Point out each Plasmodium parasite and each leukocyte.
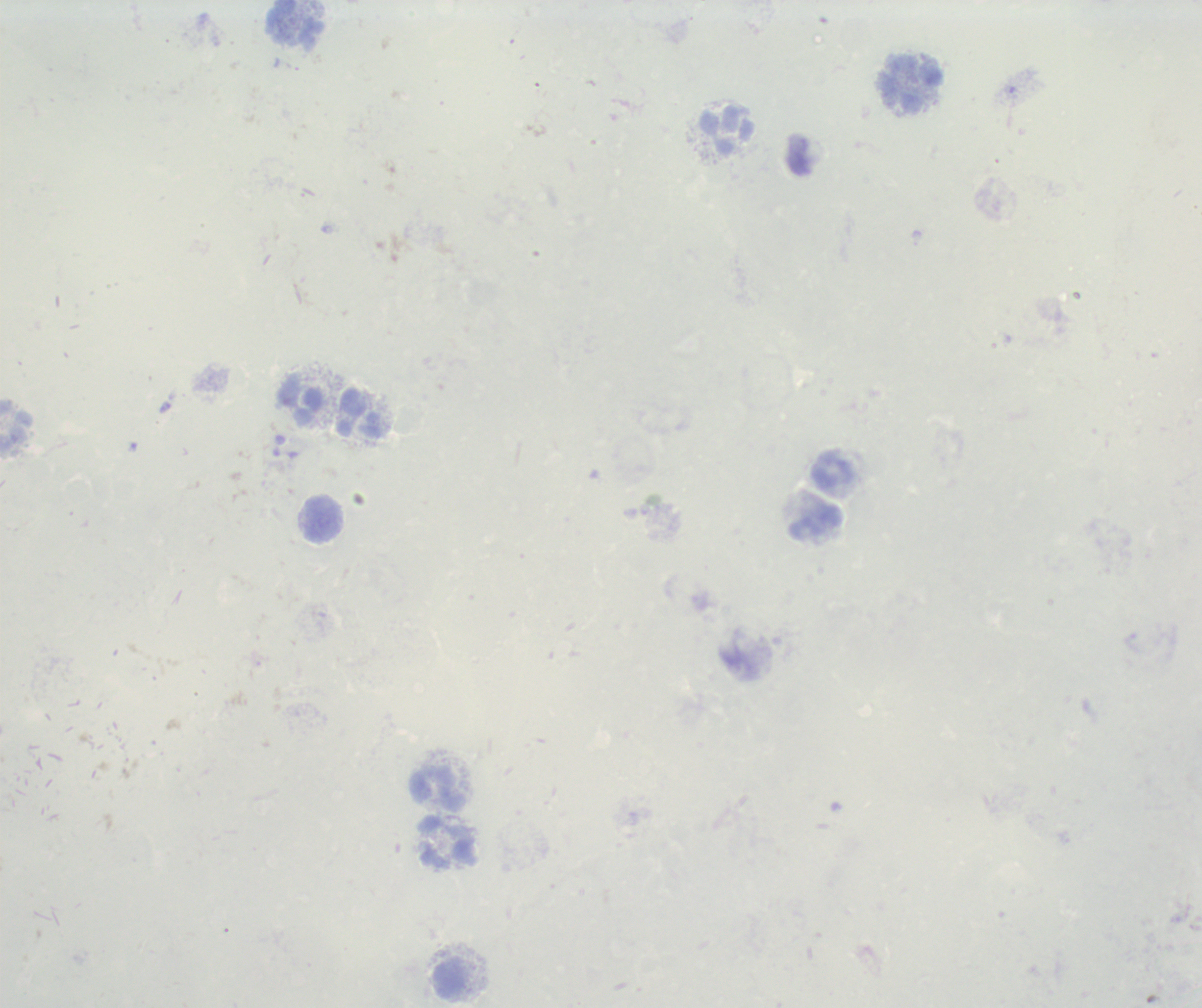

No Plasmodium parasites seen.
Approximate object centers, in pixels from the top-left corner.
Leukocytes: (x=295, y=23), (x=911, y=83), (x=727, y=130), (x=301, y=402), (x=360, y=415), (x=834, y=471), (x=322, y=518), (x=815, y=522), (x=438, y=790), (x=448, y=841), (x=450, y=979).

field of view = one from this slide
background quality = poor
magnification = 100x
image size = 1202×1008 pixels
stain = Romanowsky
preparation = thick blood smear
context = previously used in an actual diagnosis